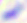
Summary:
  - Magnification: 400x
  - Identification: Toxoplasma gondii
  - Modality: micrograph